Identify the parasite.
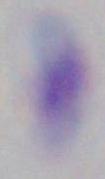
Toxoplasma gondii.

magnification = 1000x
modality = photomicrograph